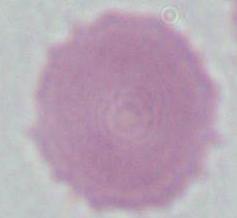

identification = erythrocyte
modality = micrograph
magnification = 1000x